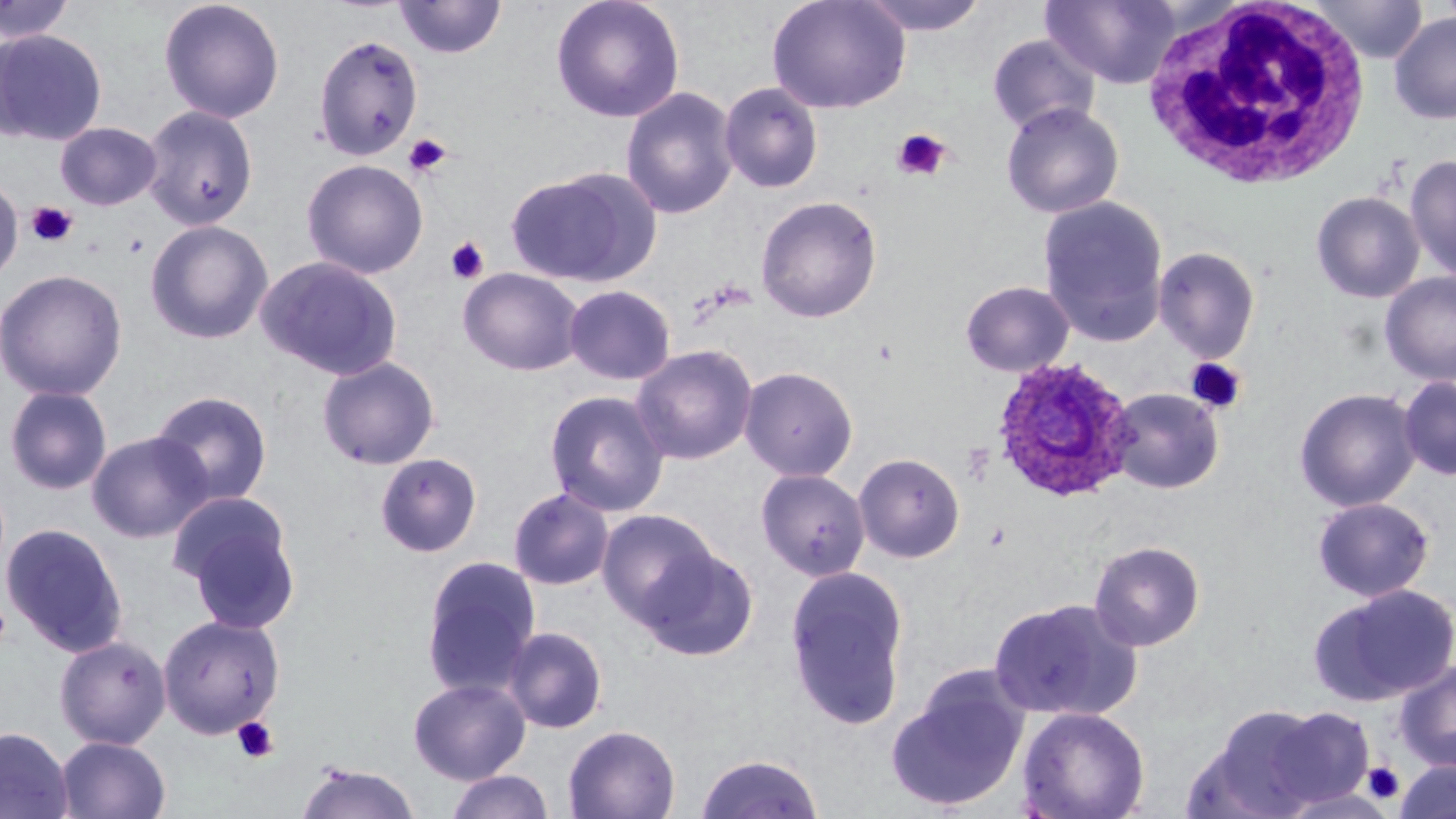

Summary:
  - Coordinate format: approximate bounding boxes as [x1, y1, x2, y2] in pixels
  - Plasmodium ovale-infected red blood cell locations: [991, 357, 1137, 503]
  - Platelet locations: [891, 128, 952, 182], [402, 134, 451, 179], [26, 202, 78, 248], [446, 237, 490, 284], [1185, 357, 1247, 414], [0, 595, 12, 653], [231, 716, 279, 764], [1362, 761, 1405, 805]
  - Uninfected red blood cell locations: [0, 0, 76, 44], [158, 0, 285, 123], [394, 0, 507, 60], [550, 0, 685, 123], [767, 0, 911, 115], [858, 0, 989, 36], [1041, 0, 1182, 89], [1309, 0, 1428, 64], [1388, 11, 1456, 125], [0, 28, 108, 146], [312, 33, 424, 160], [987, 33, 1101, 136], [719, 82, 824, 194], [620, 86, 739, 221], [1000, 101, 1124, 219], [142, 104, 259, 230], [55, 122, 162, 210], [1404, 154, 1456, 284], [301, 158, 428, 279], [507, 168, 657, 287], [0, 175, 23, 285], [1311, 191, 1425, 303], [755, 195, 883, 323], [1038, 195, 1170, 347], [144, 219, 274, 345], [1153, 245, 1261, 362], [255, 256, 403, 380], [458, 267, 585, 376], [0, 269, 127, 401], [1379, 271, 1456, 386], [959, 280, 1075, 377], [564, 284, 676, 385], [630, 344, 758, 465], [316, 356, 440, 470], [739, 366, 858, 481], [1398, 375, 1456, 481], [3, 385, 113, 495], [1294, 387, 1422, 512], [1107, 388, 1224, 494], [149, 389, 274, 508], [544, 390, 670, 516], [86, 430, 213, 543], [374, 452, 483, 558], [853, 452, 965, 563], [756, 468, 870, 580], [508, 487, 615, 591], [169, 492, 301, 631], [1312, 497, 1435, 602], [597, 509, 722, 630], [1, 522, 128, 657], [1088, 540, 1206, 651], [635, 544, 758, 660], [420, 555, 541, 699], [785, 566, 910, 730], [1309, 583, 1456, 706], [987, 597, 1140, 722], [157, 613, 286, 739], [503, 626, 608, 734], [54, 634, 172, 749], [1395, 661, 1456, 772], [887, 669, 1030, 812], [408, 677, 531, 783], [1195, 705, 1331, 818], [1017, 706, 1150, 819], [1262, 706, 1375, 809], [563, 724, 681, 818], [0, 726, 73, 818], [55, 735, 171, 819], [695, 752, 823, 819], [1394, 760, 1456, 819], [294, 761, 421, 819], [443, 770, 556, 819]
  - White blood cell locations: [1142, 1, 1373, 189]
  - Slide-level diagnosis: Plasmodium ovale
  - Field of view: single
  - Preparation: thin blood film
  - Magnification: 1000x
  - Image size: 1456×819 pixels
  - Stain: May-Grünwald-Giemsa
  - Modality: optical microscopy